Give the extent of all uninfected red blood cells.
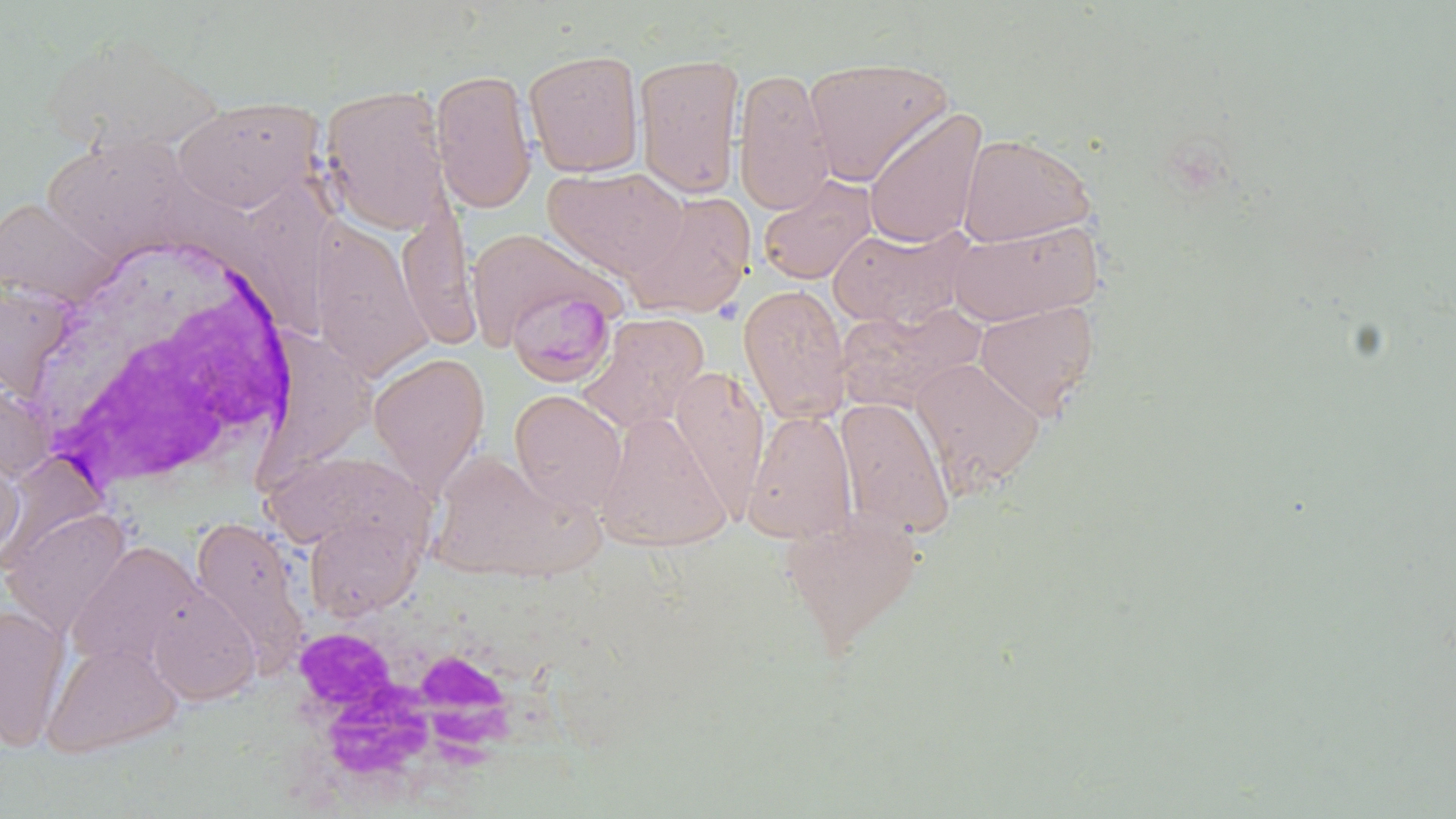
Approximate bounding boxes as named x1/y1/x2/y2 corners in pixels.
Uninfected red blood cells: (x1=38, y1=30, x2=226, y2=155), (x1=523, y1=48, x2=644, y2=177), (x1=634, y1=52, x2=745, y2=200), (x1=802, y1=55, x2=955, y2=185), (x1=733, y1=67, x2=836, y2=216), (x1=431, y1=68, x2=536, y2=215), (x1=318, y1=84, x2=453, y2=235), (x1=171, y1=97, x2=323, y2=214), (x1=863, y1=107, x2=987, y2=252), (x1=957, y1=132, x2=1095, y2=247), (x1=42, y1=134, x2=209, y2=264), (x1=543, y1=166, x2=688, y2=281), (x1=758, y1=175, x2=877, y2=285), (x1=624, y1=192, x2=756, y2=320), (x1=0, y1=196, x2=124, y2=309), (x1=397, y1=196, x2=480, y2=353), (x1=945, y1=219, x2=1102, y2=325), (x1=309, y1=221, x2=434, y2=380), (x1=828, y1=223, x2=974, y2=330), (x1=465, y1=227, x2=622, y2=353), (x1=0, y1=276, x2=80, y2=405), (x1=738, y1=284, x2=852, y2=424), (x1=974, y1=299, x2=1099, y2=419), (x1=579, y1=313, x2=710, y2=435), (x1=369, y1=353, x2=489, y2=498), (x1=910, y1=356, x2=1044, y2=496), (x1=669, y1=365, x2=769, y2=516), (x1=509, y1=389, x2=627, y2=516), (x1=834, y1=396, x2=955, y2=538), (x1=743, y1=407, x2=858, y2=544), (x1=595, y1=409, x2=732, y2=550), (x1=0, y1=446, x2=24, y2=566), (x1=264, y1=450, x2=432, y2=559), (x1=440, y1=454, x2=607, y2=586), (x1=780, y1=504, x2=924, y2=654), (x1=1, y1=506, x2=132, y2=638), (x1=304, y1=512, x2=423, y2=621), (x1=188, y1=516, x2=311, y2=673), (x1=67, y1=541, x2=206, y2=674), (x1=147, y1=584, x2=260, y2=706), (x1=0, y1=603, x2=71, y2=751), (x1=42, y1=641, x2=182, y2=758).

Summary:
  - Plasmodium malariae-infected red blood cell locations: (x1=504, y1=290, x2=617, y2=388)
  - White blood cell locations: (x1=21, y1=233, x2=304, y2=500), (x1=279, y1=587, x2=553, y2=800)
  - Slide-level diagnosis: Plasmodium malariae
  - Preparation: thin blood smear
  - Image size: 1456×819 pixels
  - Field of view: one of a larger specimen
  - Modality: optical microscopy
  - Stain: May-Grünwald-Giemsa
  - Magnification: 1000x